Give the position of every Plasmodium parasite visible.
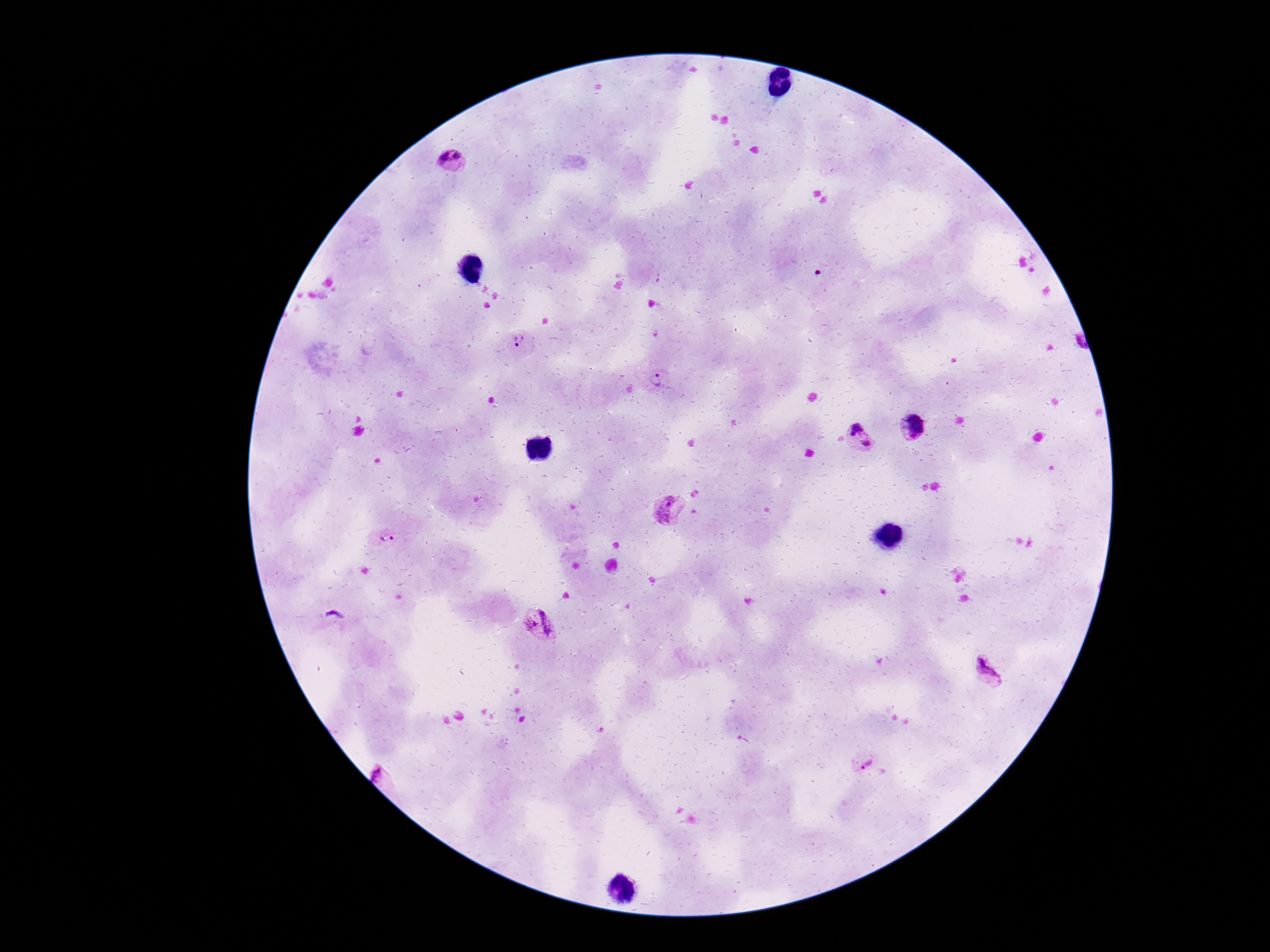

Approximate object centers, in pixels from the top-left corner.
Plasmodium parasites: (x=456, y=161), (x=518, y=343), (x=657, y=381), (x=917, y=427), (x=858, y=439), (x=668, y=511), (x=384, y=536), (x=536, y=624), (x=988, y=674), (x=866, y=762).

Patient malaria status: positive. One field from this slide. Thick blood film. Photographed through the microscope eyepiece with a smartphone camera. Giemsa stain. 100x magnification. Image is 1270×952 pixels.